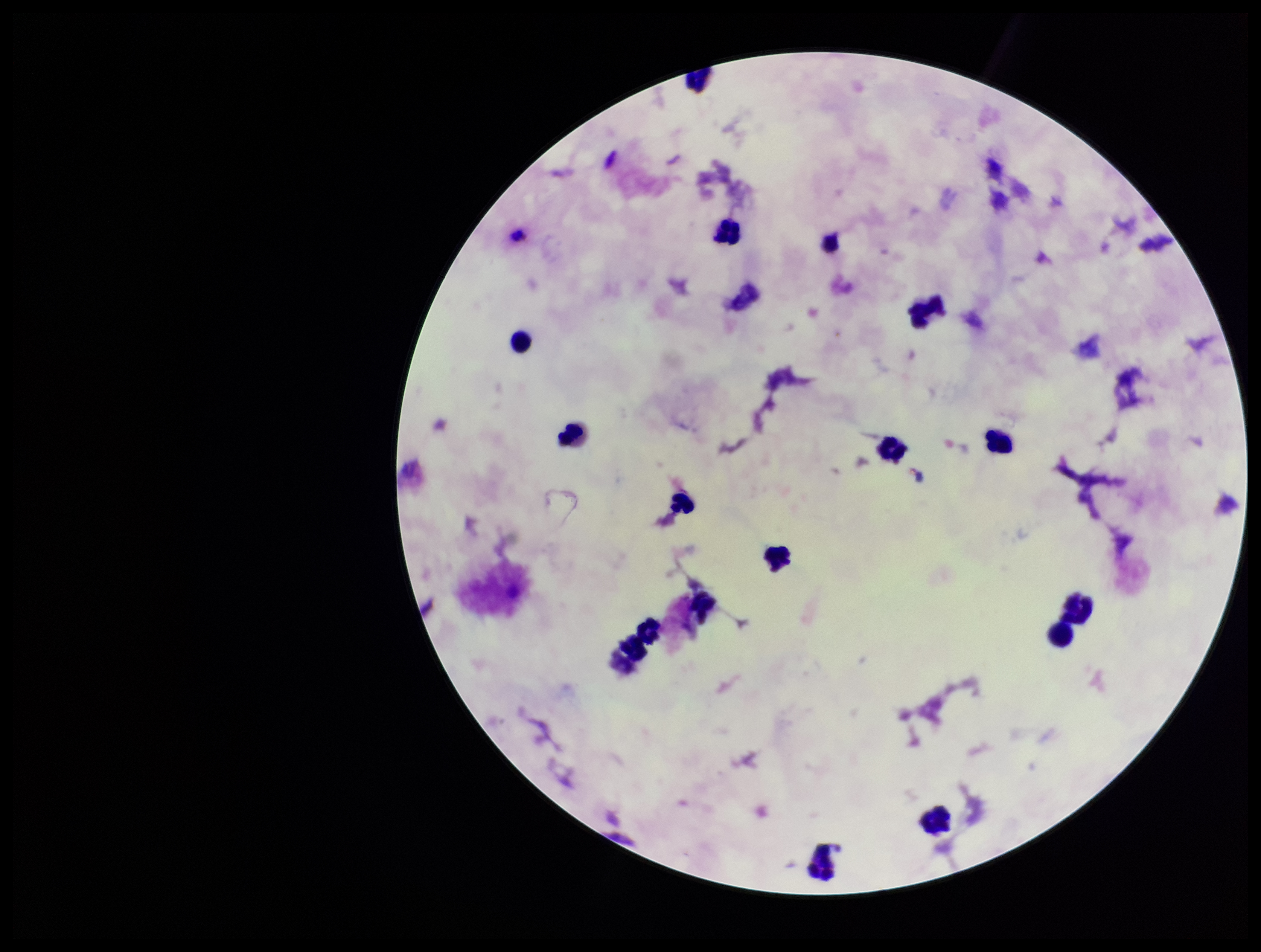

Summary:
  - Patient malaria status: negative
  - Parasite count: 0
  - Preparation: thick blood smear
  - Plasmodium parasites: none seen
  - Capture: smartphone photograph through the microscope eyepiece
  - Image size: 1261×952 pixels
  - Stain: Giemsa
  - Field of view: one from this slide
  - Leukocyte count: 16